Name the blood parasite species.
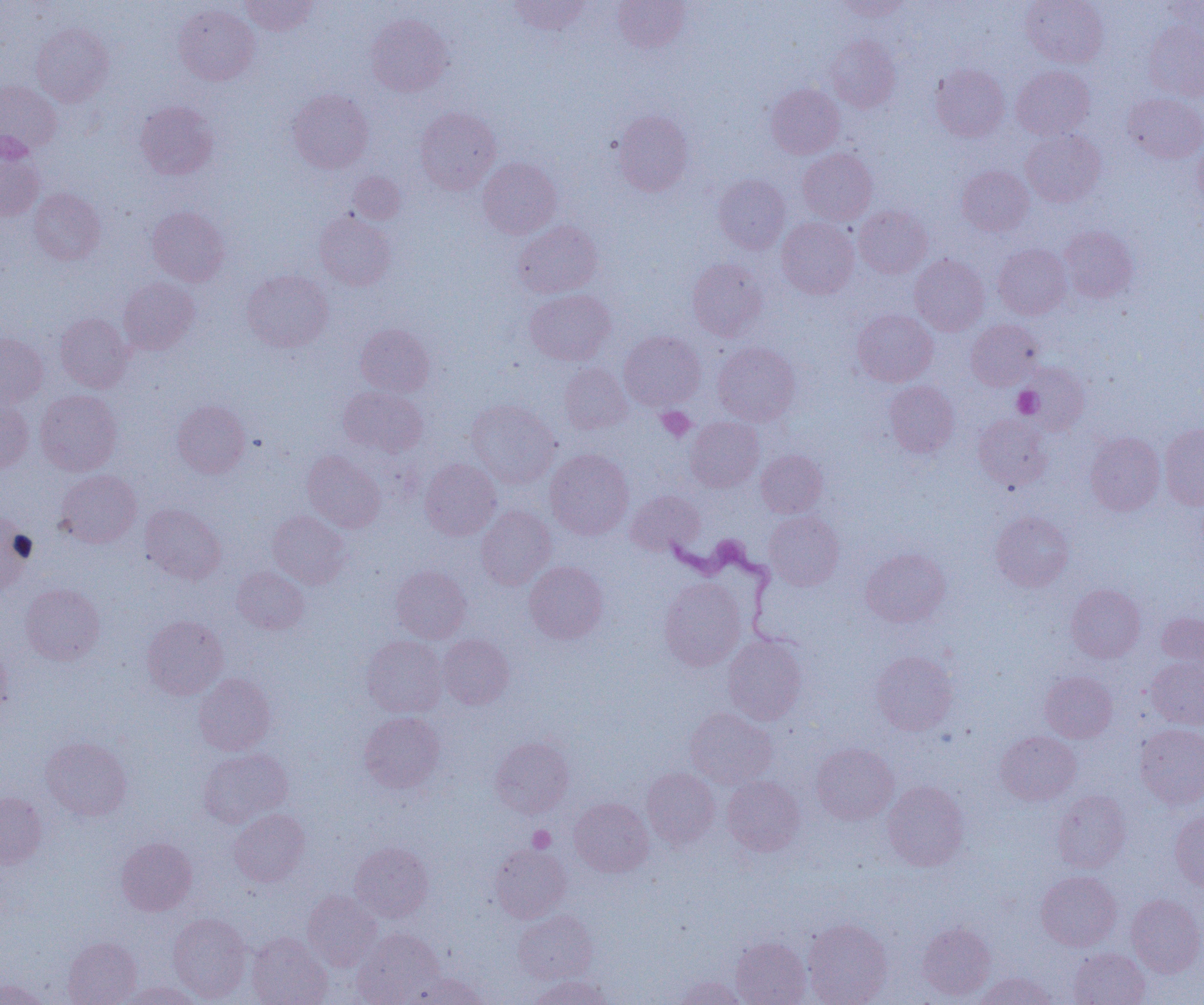
Trypanosoma brucei.

Approximate bounding boxes as (x1,y1)-(x2,y2) corner pairs in pixels. Uninfected red blood cell locations: (241,0)-(318,35), (509,0)-(590,35), (836,0)-(912,20), (1021,0)-(1108,68), (613,1)-(690,52), (1162,2)-(1204,41), (174,4)-(259,85), (366,14)-(452,96), (1143,21)-(1204,101), (31,22)-(113,106), (826,35)-(901,113), (930,64)-(1009,141), (1011,65)-(1094,139), (0,80)-(62,155), (766,83)-(844,158), (288,88)-(374,173), (1123,93)-(1204,163), (135,101)-(218,179), (416,107)-(500,194), (613,110)-(694,196), (1021,129)-(1106,206), (1193,139)-(1204,208), (0,142)-(44,221), (798,149)-(877,224), (478,157)-(561,238), (957,165)-(1033,235), (349,172)-(405,224), (714,174)-(790,253), (29,187)-(106,264), (854,205)-(932,278), (147,206)-(230,286), (314,210)-(395,290), (777,217)-(859,298), (514,221)-(603,298), (1059,226)-(1137,302), (993,244)-(1072,319), (909,254)-(989,335), (687,259)-(767,340), (242,270)-(333,352), (118,277)-(199,354), (525,289)-(615,365), (852,309)-(937,387), (55,313)-(133,392), (966,319)-(1043,390), (355,324)-(434,396), (619,331)-(705,410), (0,333)-(48,408), (713,343)-(801,425), (1018,362)-(1090,434), (559,363)-(632,433), (884,381)-(959,458), (339,386)-(428,457), (35,389)-(122,475), (0,400)-(34,472), (172,400)-(250,477), (467,400)-(561,488), (973,414)-(1053,492), (685,416)-(764,492), (1159,424)-(1204,510), (1085,432)-(1165,515), (545,448)-(634,539), (756,449)-(827,517), (302,451)-(385,532), (420,458)-(501,540), (56,470)-(141,547), (626,490)-(704,555), (140,503)-(225,584), (477,506)-(555,590), (268,511)-(351,589), (764,511)-(844,590), (990,511)-(1073,592), (0,514)-(36,594), (861,548)-(951,627), (524,561)-(608,644), (390,565)-(471,643), (232,566)-(309,634), (659,577)-(746,670), (20,583)-(105,666), (1066,584)-(1145,663), (1157,612)-(1203,669), (142,615)-(228,699), (438,634)-(515,709), (723,635)-(808,725), (361,636)-(447,717), (0,644)-(11,715), (871,650)-(958,735), (1146,657)-(1204,728), (1040,671)-(1117,742), (194,673)-(276,755), (685,707)-(777,787), (359,711)-(445,793), (1135,723)-(1204,809), (995,731)-(1081,804), (41,737)-(131,820), (490,737)-(574,817), (810,743)-(899,824), (199,749)-(292,828), (642,768)-(719,848), (721,776)-(805,856), (882,780)-(969,870), (1052,790)-(1131,873), (0,792)-(47,867), (569,798)-(654,877), (230,809)-(310,886), (1170,810)-(1204,891), (116,837)-(197,915), (350,843)-(433,922), (490,844)-(571,922), (1036,871)-(1121,950), (303,890)-(381,971), (1127,894)-(1204,977), (513,910)-(597,983), (168,913)-(251,1002), (803,919)-(893,1005), (917,922)-(995,1001), (354,928)-(445,1004), (247,933)-(332,1005), (731,936)-(811,1005), (63,937)-(141,1005), (1068,948)-(1150,1005), (409,972)-(489,1004), (973,972)-(1058,1005), (530,974)-(611,1005), (673,976)-(748,1005), (0,979)-(47,1005), (120,981)-(204,1005). Platelet locations: (1012,386)-(1043,418), (657,407)-(695,441), (528,826)-(555,852). Trypanosoma brucei locations: (659,531)-(785,644). Image is 1204×1005 pixels. Thin blood film. Captured at 1000x magnification. One field of a larger specimen. Optical microscopy.